Report the malaria status of this cell.
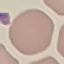
It is uninfected.

Automatically extracted cell patch, resized to 64 × 64 pixels. Giemsa-stained preparation. Thin blood film. Photographed with a smartphone camera at the microscope eyepiece.